Locate every malaria parasite.
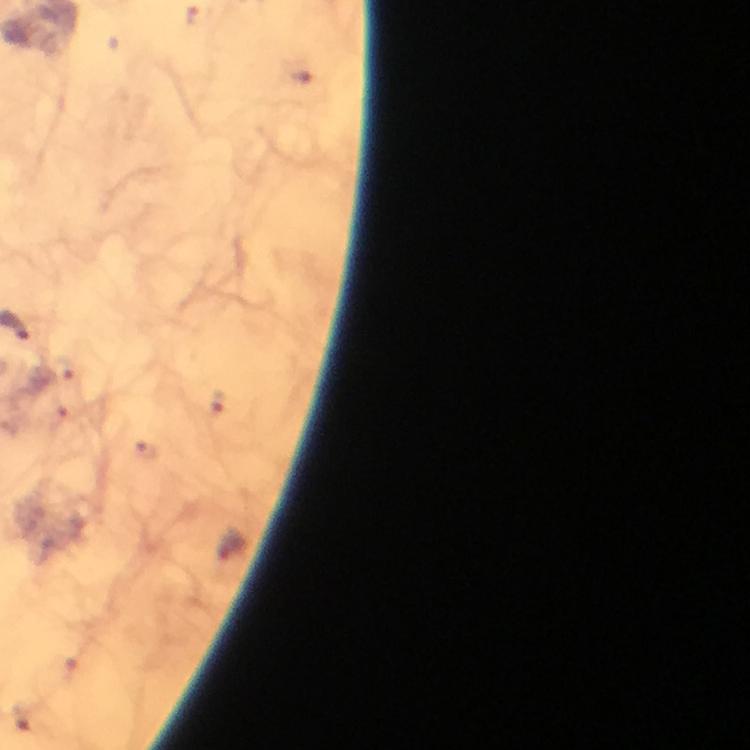

Approximate centers as {x, y} in pixels.
Malaria parasites: {201, 17}, {300, 76}, {65, 370}, {221, 402}.

{
  "image_size": "750×750 pixels",
  "capture": "smartphone photograph through a microscope",
  "magnification": "100x",
  "context": "from a malaria diagnostic workup",
  "preparation": "thick blood smear",
  "immersion_oil": "applied",
  "cropped_from": "one field of view",
  "stain": "Giemsa"
}